Classify this cell by malaria status.
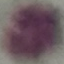
Uninfected.

capture: smartphone through the microscope eyepiece
image_type: automatically extracted cell patch, resized to 64 × 64 pixels
preparation: thin smear
stain: Giemsa